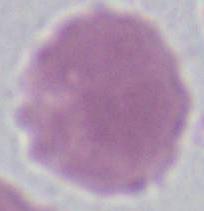

Captured at 1000x magnification. Photomicrograph. An erythrocyte is seen.